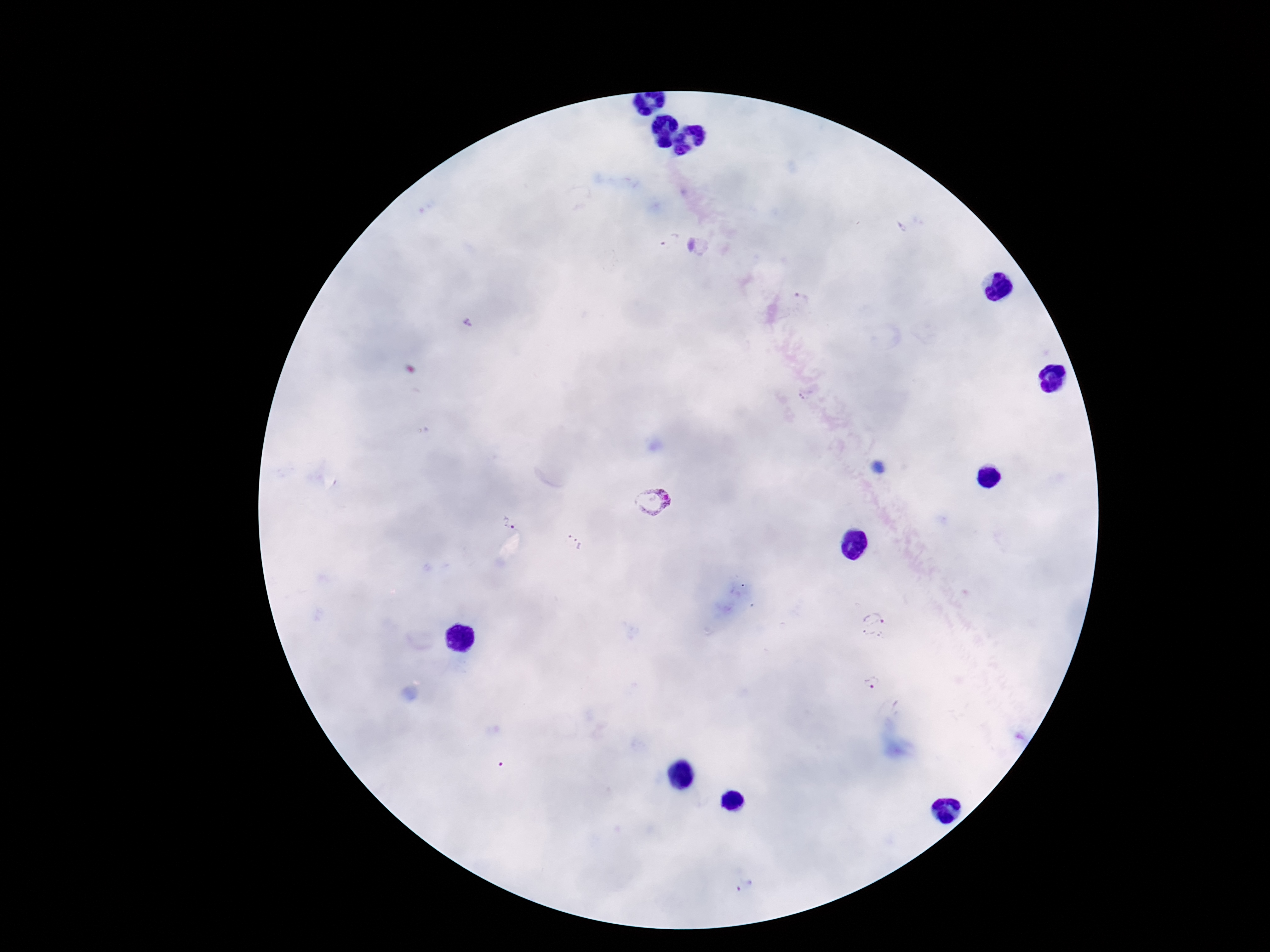

Approximate centers as (x, y) in pixels.
Summary:
  - Plasmodium parasite locations: (656, 501), (503, 519), (573, 544), (872, 627), (872, 682)
  - Image size: 1270×952 pixels
  - Magnification: 100x
  - Capture: smartphone camera through the microscope eyepiece
  - Preparation: thick blood smear
  - Patient malaria status: infected
  - Field of view: one from this slide
  - Stain: Giemsa